Locate every Plasmodium parasite.
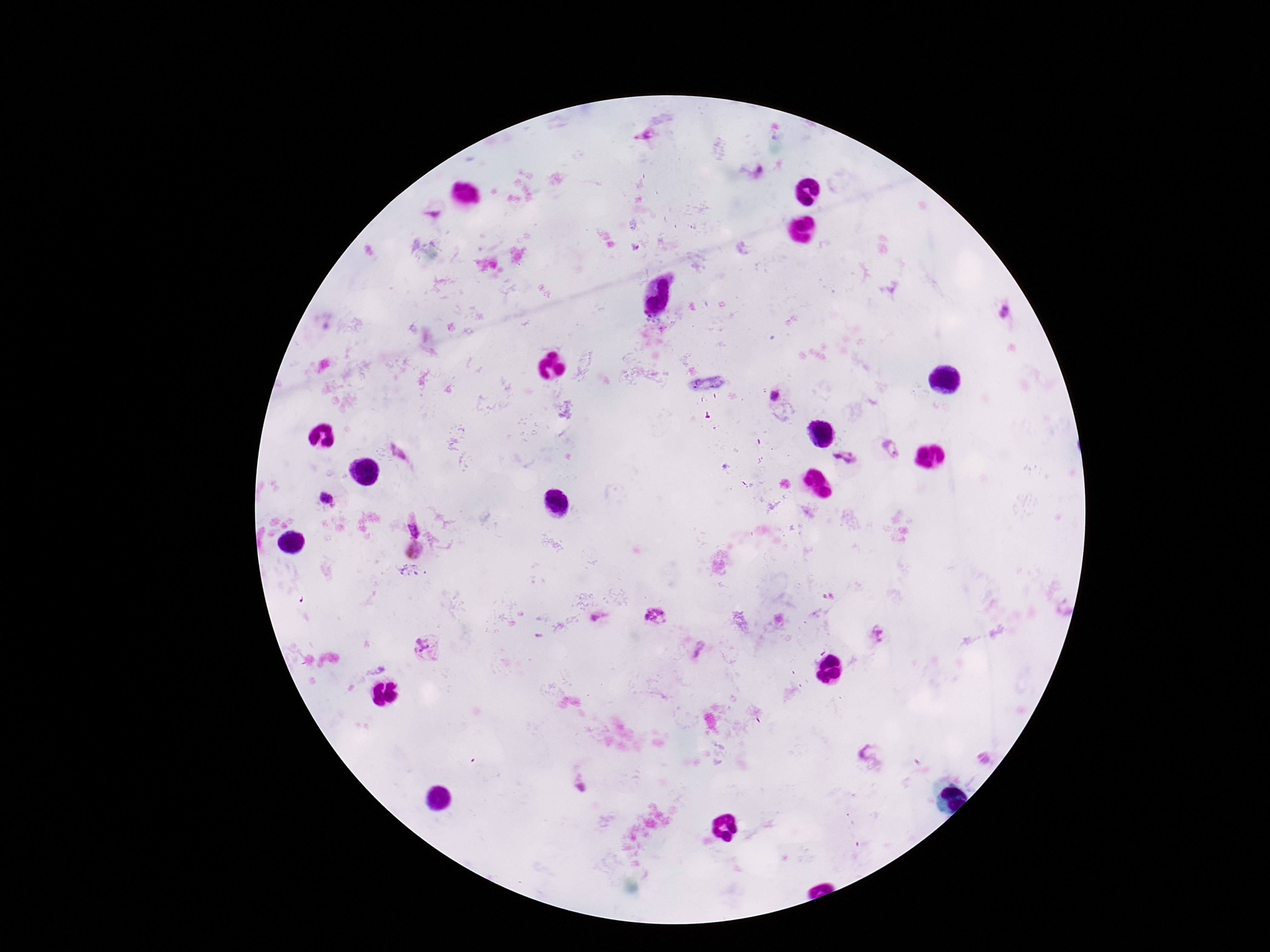

Approximate centers as (x, y) in pixels.
Plasmodium parasites: (644, 138), (1005, 311), (776, 396), (891, 449), (842, 458), (325, 498), (413, 528), (415, 550), (655, 617), (598, 618), (428, 648), (871, 757), (582, 788).

field of view = single
magnification = 100x
stain = Giemsa
patient malaria status = positive
image size = 1270×952 pixels
capture = smartphone camera through the microscope eyepiece
preparation = thick blood film